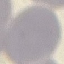

{
  "malaria_status": "uninfected",
  "capture": "smartphone through the microscope eyepiece",
  "stain": "Giemsa",
  "preparation": "thin blood smear",
  "image_type": "automatically extracted cell patch, resized to 64 × 64 pixels"
}